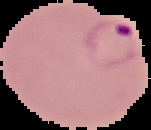
Summary:
  - Image type: segmented cell region on a black background
  - Malaria status: parasitized
  - Image size: 151×130 pixels
  - Preparation: thin blood smear